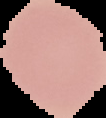
preparation = thin blood smear
image type = segmented cell region with the area outside set to black
image size = 106×118 pixels
malaria status = uninfected